Assess this cell for malaria.
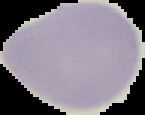
It is uninfected.

Summary:
  - Image size: 145×115 pixels
  - Image type: cell region segmented out of the field of view; surrounding area masked to black
  - Preparation: thin blood film